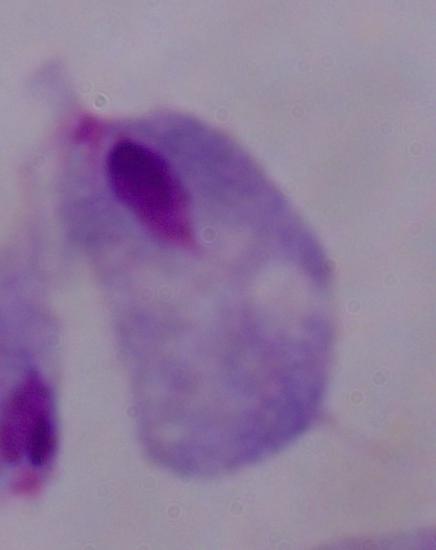 Photomicrograph. A trichomonad is shown. Captured at 1000x magnification.